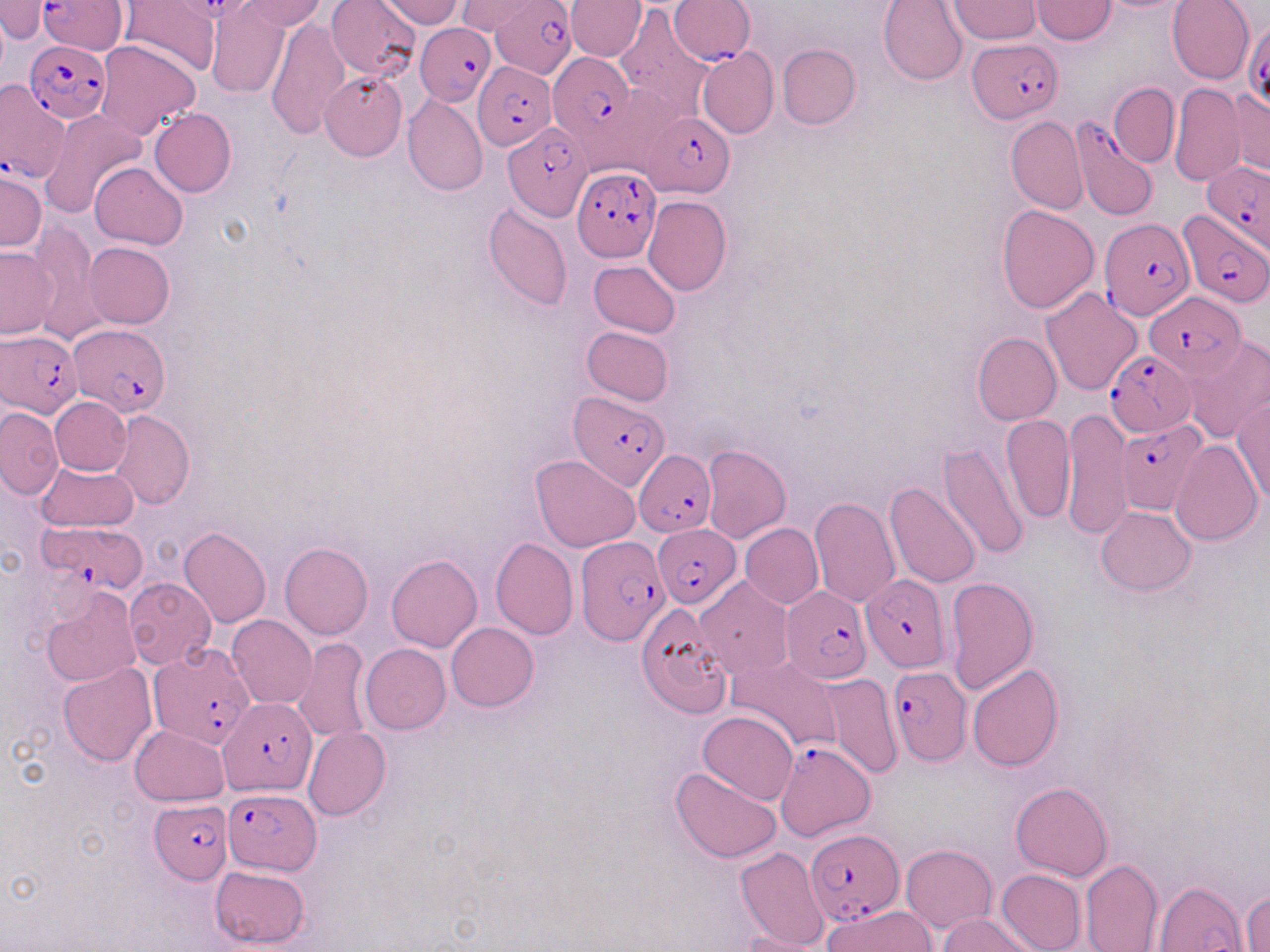 Approximate bounding boxes as [x1, y1, x2, y2] in pixels. Uninfected red blood cell locations: [2, 0, 51, 40], [118, 0, 220, 78], [236, 0, 328, 31], [326, 0, 420, 82], [378, 0, 467, 25], [565, 0, 646, 61], [879, 0, 968, 84], [1029, 0, 1117, 44], [1167, 0, 1254, 85], [454, 1, 541, 35], [948, 1, 1042, 43], [205, 3, 291, 98], [613, 6, 714, 121], [265, 17, 349, 138], [94, 40, 201, 140], [777, 44, 860, 129], [696, 46, 778, 138], [319, 70, 407, 161], [1109, 82, 1179, 167], [1168, 82, 1245, 185], [1228, 86, 1270, 177], [402, 95, 489, 195], [39, 109, 147, 219], [149, 109, 236, 198], [1006, 116, 1086, 214], [90, 161, 187, 248], [0, 169, 45, 253], [643, 197, 732, 295], [483, 202, 572, 312], [996, 203, 1099, 313], [29, 219, 106, 342], [84, 242, 175, 328], [1, 246, 58, 338], [590, 260, 680, 337], [1041, 286, 1142, 395], [582, 326, 673, 407], [972, 331, 1062, 425], [1179, 335, 1270, 445], [50, 396, 131, 476], [1232, 397, 1270, 505], [0, 406, 63, 498], [1062, 407, 1131, 542], [108, 408, 193, 510], [1001, 412, 1075, 524], [1170, 439, 1262, 544], [935, 443, 1031, 563], [702, 445, 791, 543], [531, 455, 640, 552], [37, 460, 138, 532], [884, 481, 980, 589], [808, 495, 901, 607], [1096, 505, 1195, 595], [741, 523, 824, 609], [179, 525, 271, 627], [491, 538, 578, 640], [279, 542, 372, 639], [386, 554, 482, 652], [693, 575, 792, 679], [944, 576, 1039, 696], [123, 577, 216, 670], [40, 586, 140, 687], [638, 602, 732, 716], [228, 615, 317, 709], [446, 622, 538, 711], [294, 639, 373, 745], [360, 643, 451, 733], [728, 655, 844, 753], [57, 663, 156, 766], [967, 664, 1064, 770], [816, 671, 903, 778], [698, 711, 798, 805], [130, 725, 228, 805], [302, 726, 391, 821], [669, 767, 781, 863], [1010, 781, 1112, 881], [900, 844, 997, 932], [736, 846, 829, 949], [1079, 858, 1162, 952], [209, 865, 309, 949], [996, 868, 1086, 952], [1154, 877, 1248, 952], [1243, 891, 1269, 952], [824, 905, 935, 952], [937, 912, 1037, 952], [733, 931, 834, 952]. Plasmodium falciparum-infected red blood cell locations: [492, 0, 578, 76], [669, 0, 755, 64], [39, 1, 123, 51], [1243, 20, 1270, 111], [414, 24, 494, 105], [967, 39, 1061, 123], [24, 42, 111, 122], [550, 51, 636, 149], [473, 62, 556, 149], [0, 79, 72, 185], [644, 112, 734, 195], [1070, 117, 1157, 222], [503, 124, 592, 221], [1202, 160, 1269, 251], [573, 167, 660, 262], [1176, 209, 1268, 309], [1097, 217, 1190, 318], [1146, 292, 1246, 377], [68, 323, 171, 414], [1, 331, 83, 416], [1104, 350, 1196, 436], [572, 391, 667, 488], [1115, 419, 1208, 515], [634, 450, 714, 536], [36, 521, 147, 593], [652, 524, 741, 608], [576, 535, 670, 646], [862, 575, 950, 671], [784, 585, 873, 683], [150, 646, 256, 752], [887, 666, 972, 767], [218, 697, 316, 795], [774, 738, 878, 839], [223, 788, 321, 874], [149, 800, 231, 883], [804, 829, 902, 923]. Slide-level diagnosis: Plasmodium falciparum. Thin blood smear. Image is 1270×952 pixels. 1000x magnification. Single field of view. Optical microscopy. May-Grünwald-Giemsa-stained preparation.